Assess this cell for malaria.
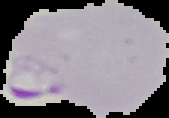
It is parasitized.

Summary:
  - Preparation: thin blood film
  - Image type: segmented cell region on a black background
  - Image size: 169×118 pixels